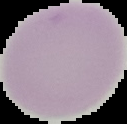

Summary:
  - Preparation: thin blood smear
  - Malaria status: uninfected
  - Image size: 127×124 pixels
  - Image type: segmented cell region with the area outside set to black